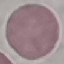 Result: no malaria parasites detected. Giemsa stain. Thin smear of blood. Automatically extracted cell patch, resized to 64 × 64 pixels. Acquired by smartphone through the microscope eyepiece.